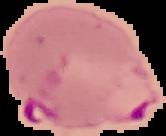
Image is 166×136 pixels. From a thin blood film. The area outside the segmented cell region is set to black. Result: Plasmodium parasites detected.